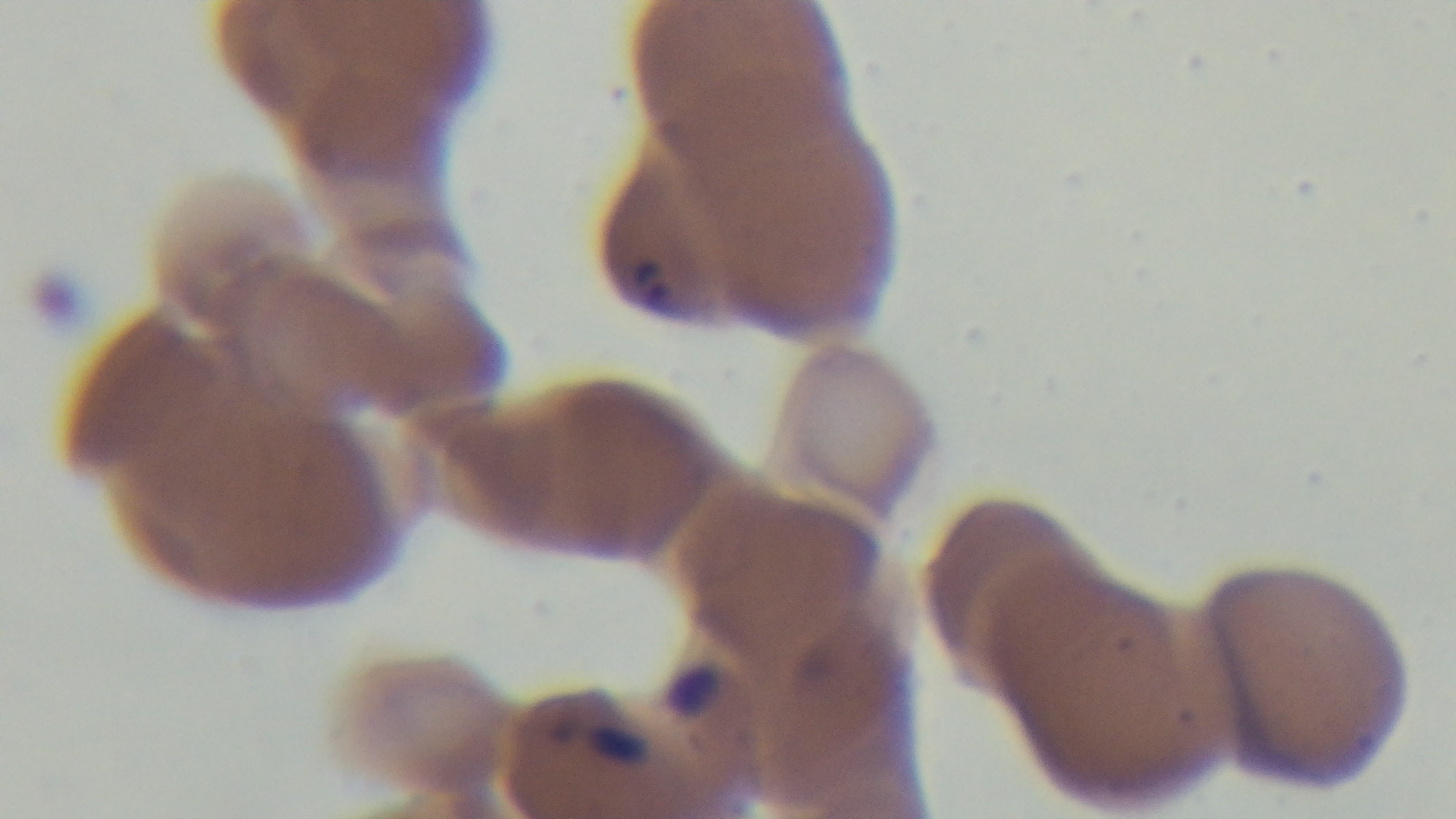
Summary:
  - Stain: Giemsa
  - Malaria status: positive
  - Capture: mounted 4K digital camera
  - Field of view: one from the slide
  - Preparation: thin
  - Modality: light microscopy
  - Objective: 100x oil immersion